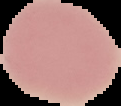

Summary:
  - Preparation: thin blood film
  - Image size: 121×106 pixels
  - Image type: segmented cell region with the area outside set to black
  - Malaria status: uninfected